Report the malaria status of this cell.
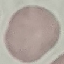

Uninfected.

image_type: cell patch, automatically extracted from a larger field of view and resized to 64 × 64 pixels
stain: Giemsa
capture: smartphone camera at the microscope eyepiece
preparation: thin smear